Assess this cell for malaria.
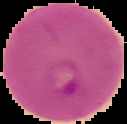
It is parasitized.

{
  "image_type": "segmented cell region on a black background",
  "image_size": "127×124 pixels",
  "preparation": "thin blood smear"
}